Name the cell type shown.
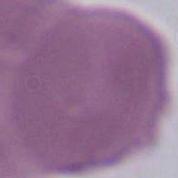
This is an erythrocyte.

1000x magnification. Photomicrograph.